Locate every malaria parasite.
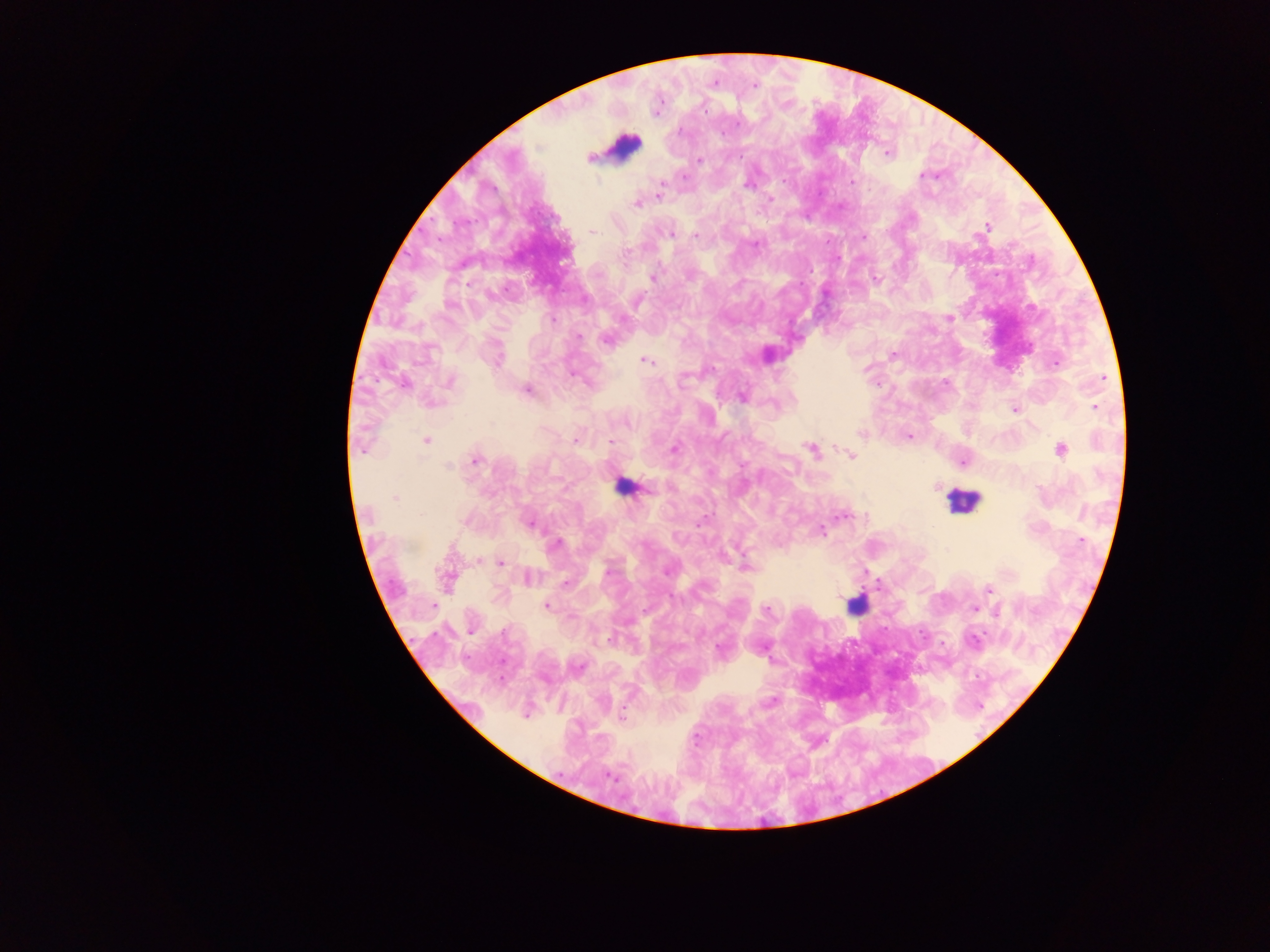
Approximate centers as [x, y] in pixels.
Malaria parasites: [755, 86], [704, 111], [737, 124], [887, 153], [590, 157], [699, 160], [684, 176], [922, 176], [661, 182], [852, 183], [748, 185], [659, 194], [770, 200], [636, 205], [987, 227], [593, 231], [670, 235], [695, 236], [863, 237], [755, 245], [652, 278], [875, 280], [639, 300], [450, 306], [949, 318], [553, 319], [622, 319], [578, 336], [606, 341], [892, 355], [645, 361], [1055, 363], [1103, 378], [450, 382], [403, 383], [526, 389], [741, 397], [1095, 407], [1015, 410], [626, 423], [861, 434], [910, 437], [426, 442], [575, 442], [611, 442], [674, 449], [811, 449], [362, 450], [1061, 450], [852, 456], [476, 461], [963, 462], [448, 465], [936, 487], [395, 498], [842, 515], [466, 522], [529, 524], [822, 532], [1082, 541], [555, 545], [500, 563], [746, 567], [608, 571], [666, 572], [529, 577], [565, 584], [988, 589], [434, 605], [547, 605], [974, 609], [767, 611], [997, 612], [472, 632], [609, 640], [974, 640], [719, 649], [771, 702], [525, 714], [622, 716], [612, 777].

Leukocyte locations: [623, 146], [622, 486], [962, 502], [853, 608]. Mobile-phone photograph taken through the microscope. One field of view. Thick blood smear. Collected in Ghana. Image is 1270×952 pixels.